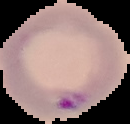

result = Plasmodium parasites detected
image type = cell region segmented out of the field of view; surrounding area masked to black
preparation = thin blood smear
image size = 130×124 pixels